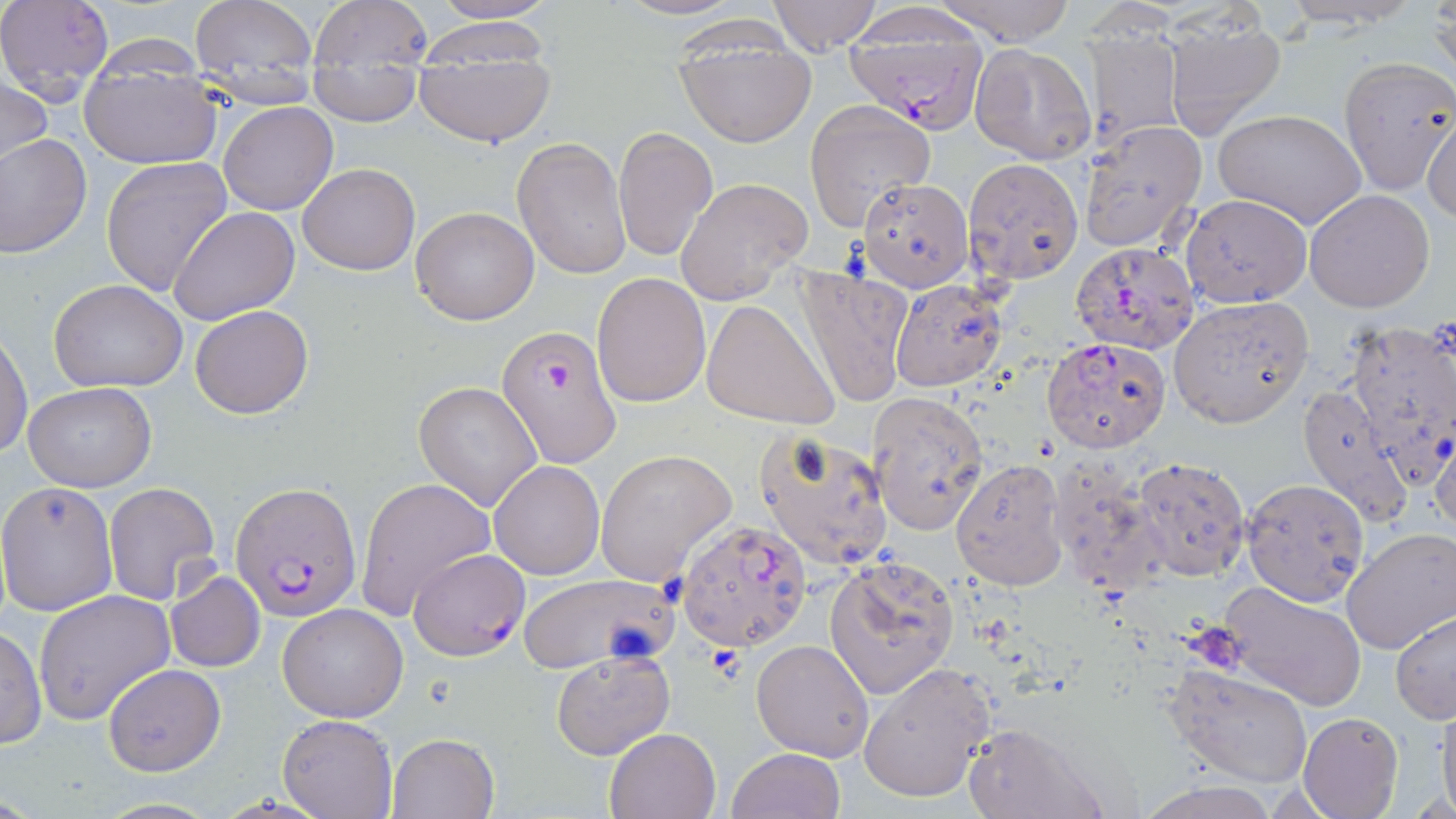

Summary:
  - Coordinate format: approximate bounding boxes as named x1/y1/x2/y2 corners in pixels
  - Plasmodium falciparum-infected red blood cell locations: (x1=845, y1=16, x2=991, y2=133), (x1=1069, y1=242, x2=1200, y2=355), (x1=496, y1=323, x2=624, y2=472), (x1=232, y1=479, x2=362, y2=622), (x1=678, y1=517, x2=814, y2=650), (x1=409, y1=549, x2=529, y2=660)
  - Uninfected red blood cell locations: (x1=0, y1=0, x2=115, y2=99), (x1=189, y1=0, x2=319, y2=98), (x1=613, y1=0, x2=745, y2=21), (x1=767, y1=0, x2=884, y2=55), (x1=928, y1=0, x2=1077, y2=45), (x1=1277, y1=0, x2=1419, y2=29), (x1=306, y1=1, x2=437, y2=81), (x1=418, y1=1, x2=559, y2=27), (x1=1426, y1=5, x2=1455, y2=83), (x1=1159, y1=9, x2=1289, y2=139), (x1=415, y1=12, x2=559, y2=59), (x1=1084, y1=18, x2=1186, y2=152), (x1=672, y1=24, x2=817, y2=147), (x1=414, y1=41, x2=556, y2=147), (x1=970, y1=42, x2=1096, y2=165), (x1=1340, y1=57, x2=1455, y2=194), (x1=310, y1=58, x2=422, y2=126), (x1=79, y1=65, x2=223, y2=168), (x1=1, y1=75, x2=52, y2=179), (x1=804, y1=100, x2=934, y2=231), (x1=219, y1=102, x2=338, y2=215), (x1=1423, y1=108, x2=1456, y2=224), (x1=1212, y1=109, x2=1366, y2=229), (x1=1080, y1=121, x2=1206, y2=251), (x1=613, y1=125, x2=718, y2=263), (x1=0, y1=133, x2=92, y2=258), (x1=513, y1=136, x2=633, y2=278), (x1=101, y1=156, x2=234, y2=296), (x1=963, y1=158, x2=1083, y2=284), (x1=297, y1=163, x2=418, y2=275), (x1=675, y1=176, x2=813, y2=304), (x1=859, y1=177, x2=974, y2=290), (x1=1304, y1=189, x2=1436, y2=312), (x1=1180, y1=194, x2=1311, y2=309), (x1=170, y1=206, x2=300, y2=325), (x1=411, y1=206, x2=539, y2=324), (x1=789, y1=263, x2=912, y2=410), (x1=591, y1=272, x2=711, y2=408), (x1=48, y1=279, x2=189, y2=392), (x1=889, y1=280, x2=1009, y2=392), (x1=1169, y1=295, x2=1313, y2=428), (x1=701, y1=298, x2=841, y2=430), (x1=190, y1=304, x2=313, y2=419), (x1=1341, y1=319, x2=1456, y2=484), (x1=0, y1=329, x2=33, y2=461), (x1=1042, y1=338, x2=1170, y2=454), (x1=413, y1=380, x2=543, y2=510), (x1=1296, y1=380, x2=1410, y2=526), (x1=25, y1=382, x2=155, y2=492), (x1=867, y1=393, x2=988, y2=535), (x1=1431, y1=423, x2=1456, y2=536), (x1=754, y1=429, x2=895, y2=571), (x1=594, y1=450, x2=735, y2=584), (x1=1131, y1=455, x2=1250, y2=580), (x1=951, y1=459, x2=1067, y2=590), (x1=1049, y1=459, x2=1163, y2=597), (x1=489, y1=460, x2=604, y2=579), (x1=355, y1=477, x2=493, y2=621), (x1=1240, y1=477, x2=1370, y2=607), (x1=1, y1=480, x2=119, y2=617), (x1=102, y1=483, x2=221, y2=606), (x1=1343, y1=528, x2=1456, y2=653), (x1=824, y1=555, x2=959, y2=700), (x1=165, y1=571, x2=265, y2=674), (x1=516, y1=574, x2=672, y2=673), (x1=1216, y1=582, x2=1366, y2=709), (x1=34, y1=590, x2=176, y2=725), (x1=276, y1=604, x2=408, y2=722), (x1=1391, y1=609, x2=1456, y2=721), (x1=0, y1=626, x2=47, y2=749), (x1=750, y1=639, x2=874, y2=761), (x1=550, y1=652, x2=674, y2=759), (x1=857, y1=661, x2=998, y2=804), (x1=1168, y1=662, x2=1314, y2=787), (x1=103, y1=664, x2=225, y2=776), (x1=1434, y1=703, x2=1456, y2=814), (x1=1298, y1=712, x2=1402, y2=819), (x1=278, y1=713, x2=397, y2=818), (x1=960, y1=721, x2=1107, y2=819), (x1=604, y1=726, x2=722, y2=819), (x1=387, y1=732, x2=499, y2=819), (x1=726, y1=748, x2=845, y2=819), (x1=1140, y1=780, x2=1280, y2=819)
  - Slide-level diagnosis: Plasmodium falciparum
  - Image size: 1456×819 pixels
  - Magnification: 1000x
  - Modality: light microscopy
  - Preparation: thin blood smear
  - Stain: May-Grünwald-Giemsa
  - Field of view: one of a larger specimen